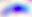

{
  "modality": "photomicrograph",
  "identification": "Toxoplasma gondii",
  "magnification": "400x"
}